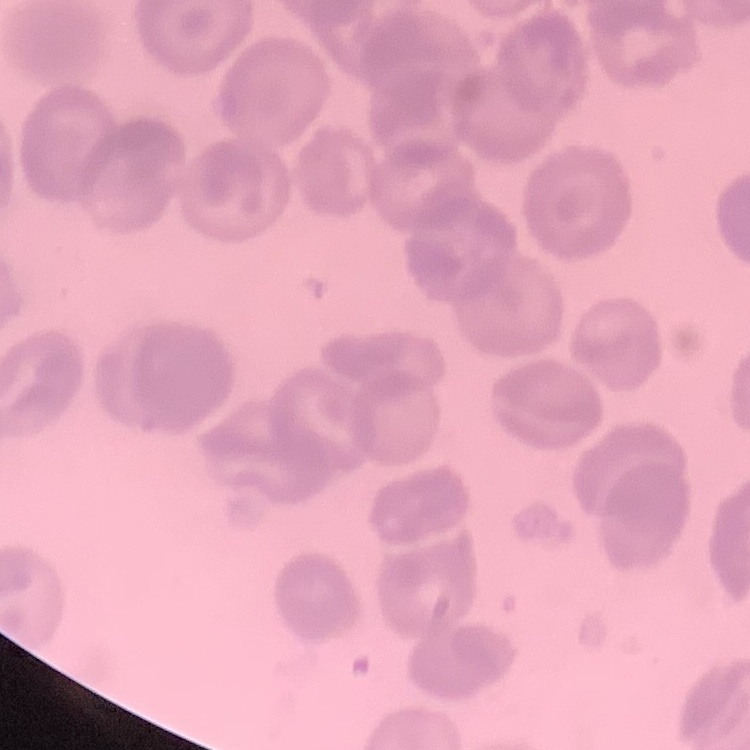

Summary:
  - Erythrocyte morphology: no rouleaux formation
  - Image type: one tile cut from a larger photomicrograph
  - Preparation: thin blood film
  - Stain: Field's or Giemsa